Locate every leukocyte (white blood cell).
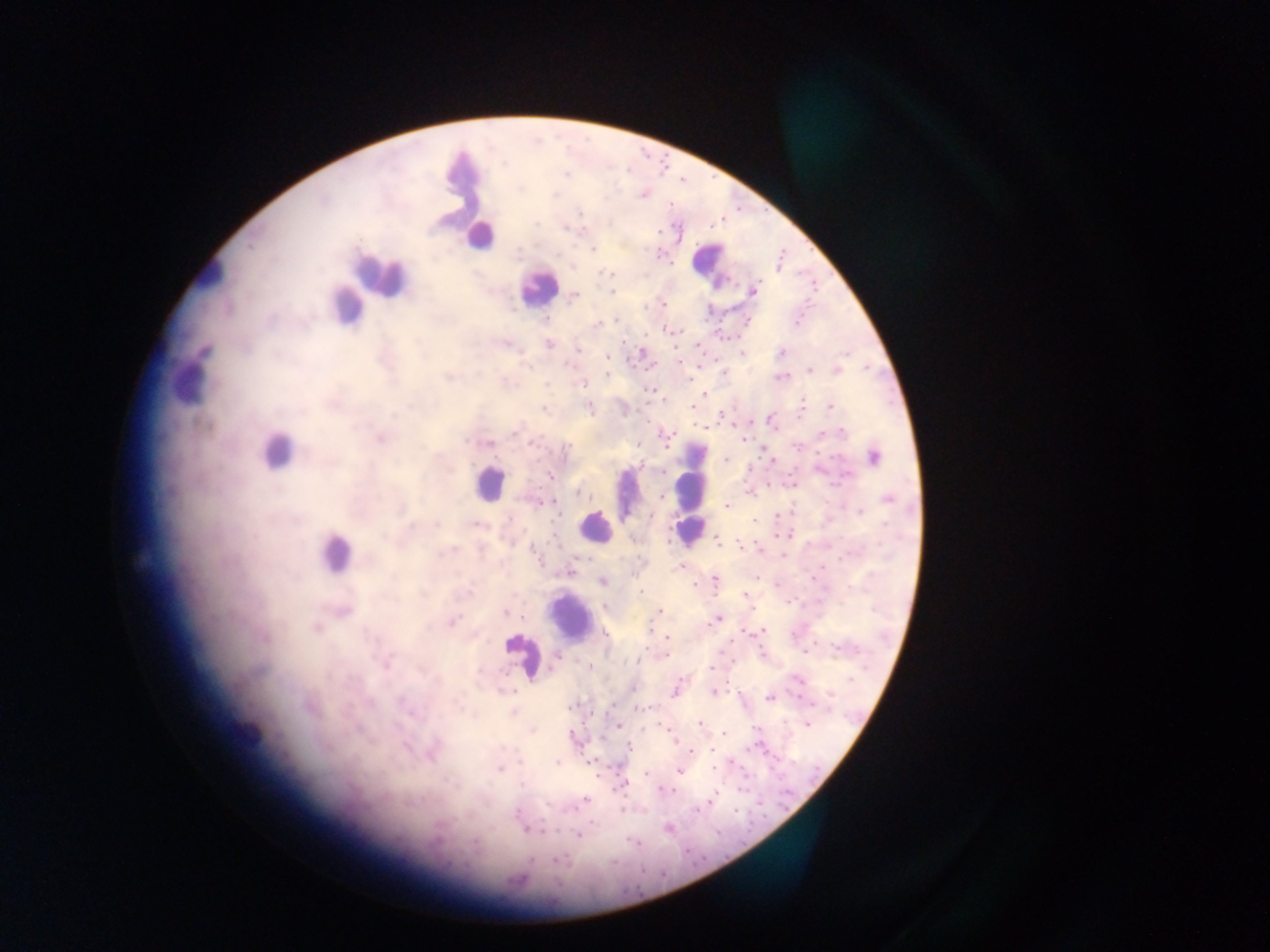

Approximate centers as [x, y] in pixels.
Leukocytes (some below the resolvable threshold): [479, 237], [710, 260], [380, 273], [208, 274], [537, 287], [345, 306], [188, 386], [275, 453], [489, 483], [628, 491], [691, 491], [595, 527], [333, 552], [570, 616], [522, 654].

Malaria parasite locations: [567, 174], [643, 194], [579, 212], [536, 223], [566, 229], [659, 231], [594, 250], [558, 255], [611, 274], [754, 290], [611, 291], [574, 296], [663, 303], [545, 318], [616, 320], [747, 321], [796, 324], [597, 325], [675, 332], [646, 335], [548, 344], [578, 349], [204, 351], [642, 352], [781, 352], [743, 354], [608, 358], [679, 361], [528, 367], [809, 371], [837, 372], [607, 374], [724, 374], [447, 378], [779, 378], [583, 384], [650, 390], [705, 395], [831, 406], [692, 407], [589, 408], [544, 410], [721, 415], [515, 433], [842, 433], [822, 434], [381, 437], [667, 440], [743, 440], [466, 441], [497, 441], [489, 443], [534, 444], [797, 446], [566, 451], [873, 458], [727, 459], [845, 476], [549, 477], [580, 492], [662, 497], [888, 500], [548, 501], [726, 506], [859, 512], [651, 516], [754, 521], [436, 524], [474, 524], [718, 542], [741, 545], [534, 550], [445, 552], [680, 566], [571, 572], [715, 580], [602, 581], [640, 592], [746, 595], [343, 611], [658, 612], [505, 613], [718, 619], [452, 621], [713, 622], [315, 629], [761, 631], [605, 634], [667, 637], [839, 648], [806, 652], [664, 655], [556, 658], [637, 661], [385, 664], [552, 666], [711, 668], [799, 680], [633, 687], [676, 689], [510, 691], [714, 692], [770, 698], [572, 707], [644, 707], [513, 713], [699, 723], [808, 724], [618, 725], [533, 730], [723, 733], [673, 737], [629, 749], [711, 749], [690, 751], [432, 757], [519, 762], [557, 762], [712, 768], [499, 770], [679, 771], [645, 774], [521, 784], [623, 784], [663, 790], [712, 799], [584, 800], [696, 809], [516, 813], [668, 829], [527, 830], [578, 835], [474, 842], [531, 860], [559, 861]. One field of view. Mobile-phone photograph taken through the microscope. Sample from Ghana. Image is 1270×952 pixels. Thick blood film.